Outline each blood parasite and name the species.
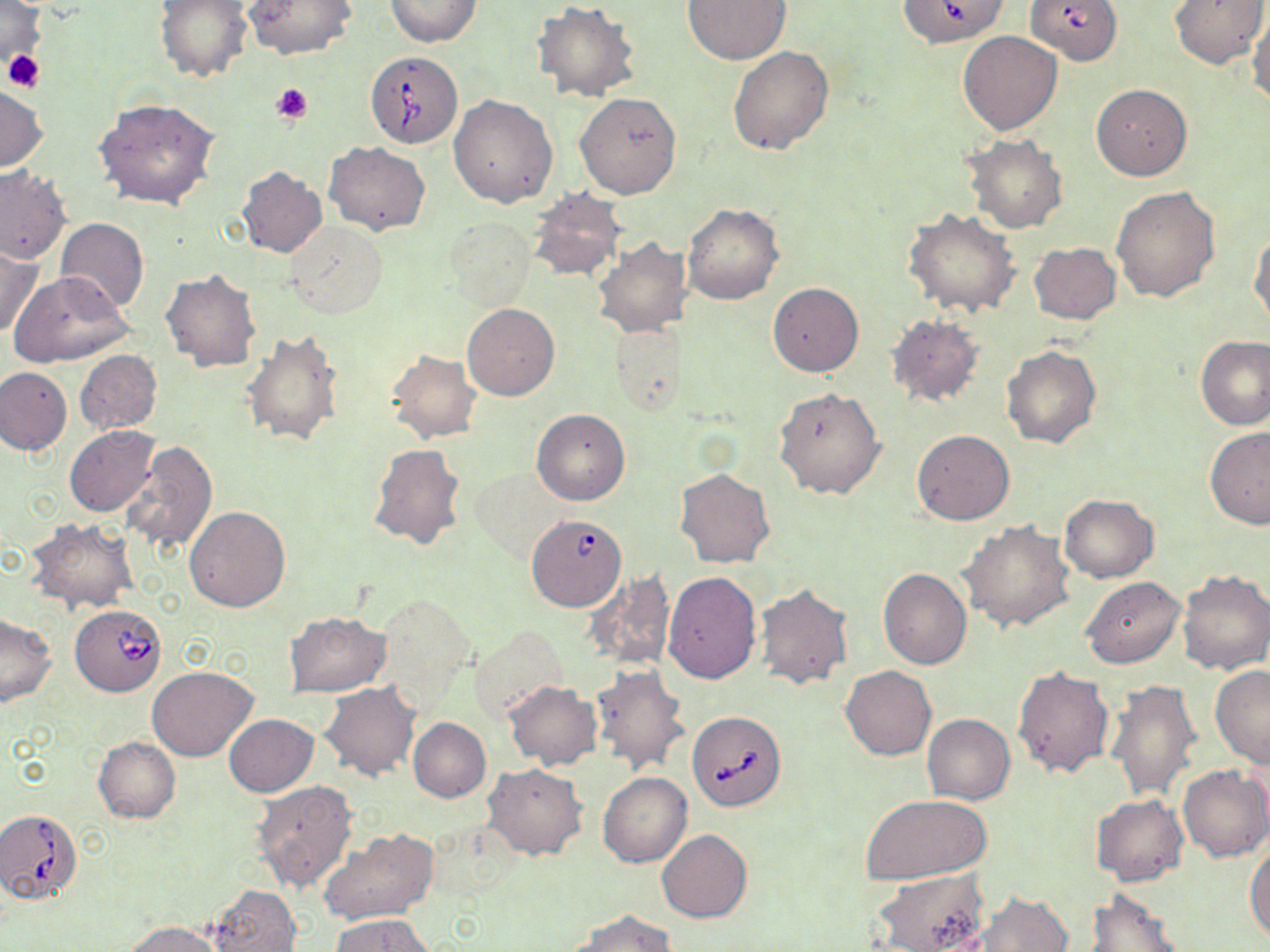
Approximate bounding boxes as (x1,y1)-(x2,y2) corner pairs in pixels.
Babesia divergens-infected red blood cells: (897,0)-(1010,47), (1025,0)-(1122,65), (364,52)-(464,149), (526,514)-(627,610), (70,603)-(167,694), (686,710)-(787,812), (0,809)-(86,903).
No Plasmodium falciparum, Plasmodium ovale, Plasmodium malariae, Plasmodium vivax, or Trypanosoma brucei observed.

Summary:
  - Platelet locations: (2,49)-(44,93), (271,82)-(314,124)
  - Uninfected red blood cell locations: (0,0)-(47,68), (154,0)-(253,83), (243,0)-(358,61), (384,0)-(481,46), (681,0)-(791,64), (1171,0)-(1268,69), (532,3)-(641,104), (1245,11)-(1269,107), (957,31)-(1064,135), (727,45)-(835,155), (1090,83)-(1193,180), (0,85)-(47,172), (575,92)-(681,199), (448,94)-(558,208), (94,98)-(221,210), (964,136)-(1067,234), (324,141)-(430,234), (0,166)-(70,265), (236,167)-(327,259), (1110,185)-(1220,303), (526,188)-(628,283), (682,204)-(784,305), (904,209)-(1020,317), (55,217)-(148,313), (445,219)-(535,310), (284,220)-(387,319), (1250,229)-(1270,328), (592,238)-(693,339), (1028,243)-(1120,324), (0,244)-(42,339), (160,269)-(262,373), (9,271)-(133,367), (767,281)-(862,376), (462,303)-(559,401), (883,313)-(986,408), (609,317)-(687,413), (242,329)-(346,449), (1196,337)-(1270,431), (1001,344)-(1101,449), (74,350)-(162,434), (387,350)-(482,443), (0,366)-(73,455), (773,387)-(885,499), (532,408)-(630,505), (65,425)-(162,517), (1203,428)-(1270,529), (911,430)-(1015,525), (118,440)-(217,556), (368,443)-(468,551), (470,468)-(566,562), (675,468)-(775,568), (1058,494)-(1159,581), (185,506)-(290,612), (28,518)-(138,612), (959,521)-(1076,633), (878,568)-(971,669), (1177,569)-(1270,674), (584,570)-(676,671), (663,571)-(761,684), (1081,577)-(1186,669), (754,583)-(854,689), (374,593)-(477,708), (0,613)-(57,706), (285,613)-(391,696), (470,626)-(567,724), (591,664)-(692,777), (1012,664)-(1115,779), (841,665)-(936,760), (147,666)-(257,761), (1210,666)-(1270,768), (1106,678)-(1201,801), (503,680)-(602,769), (320,682)-(421,781), (922,713)-(1015,805), (224,715)-(319,797), (408,717)-(491,801), (93,737)-(180,822), (483,764)-(587,859), (1178,765)-(1270,861), (598,773)-(692,867), (250,781)-(360,893), (858,793)-(993,885), (1090,795)-(1188,885), (318,827)-(437,927), (657,830)-(751,923), (1244,843)-(1270,943), (873,870)-(988,952), (209,884)-(301,952), (1085,889)-(1185,952), (978,891)-(1073,952), (570,910)-(676,952), (331,916)-(433,952), (125,921)-(223,952)
  - Slide-level diagnosis: Babesia divergens
  - Field of view: single
  - Image size: 1270×952 pixels
  - Magnification: 1000x
  - Stain: May-Grünwald-Giemsa
  - Modality: light microscopy
  - Preparation: thin blood film